Give the extent of all Plasmodium vivax-infected red blood cells.
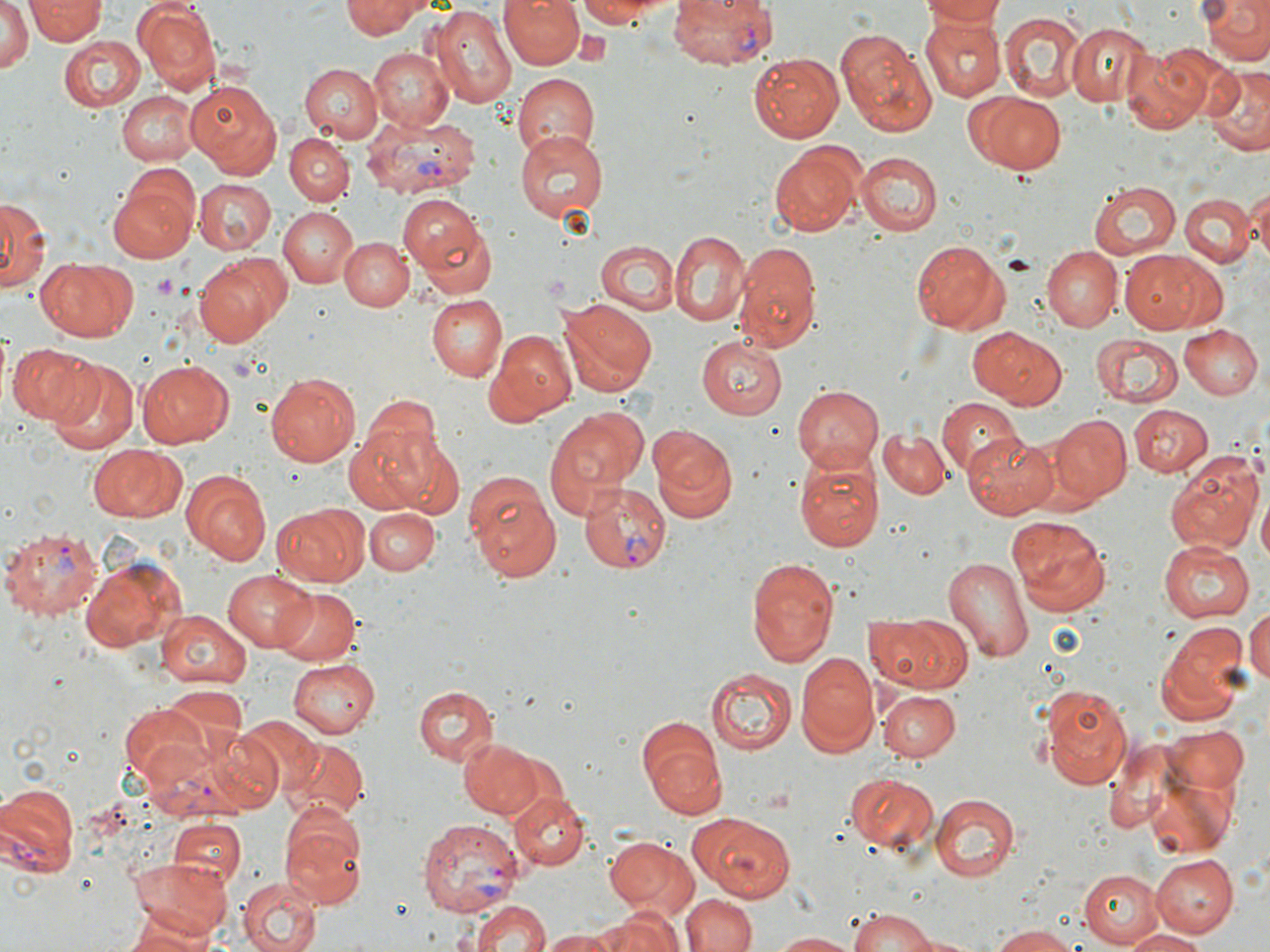
Approximate bounding boxes as (x1, y1, x2, y2) in pixels.
Plasmodium vivax-infected red blood cells: (667, 0, 778, 71), (361, 110, 480, 199), (578, 482, 672, 573), (1, 524, 104, 616), (137, 728, 276, 818), (0, 784, 79, 883), (418, 816, 523, 919).

Uninfected red blood cell locations: (26, 0, 105, 43), (339, 0, 426, 37), (501, 0, 586, 71), (573, 0, 676, 26), (918, 0, 1008, 28), (1196, 0, 1270, 67), (132, 1, 221, 95), (0, 4, 35, 73), (430, 5, 517, 106), (997, 10, 1086, 102), (919, 17, 1004, 100), (1065, 22, 1153, 109), (833, 28, 937, 138), (56, 35, 147, 111), (369, 46, 454, 131), (1122, 46, 1214, 134), (748, 53, 845, 142), (299, 63, 383, 142), (1202, 67, 1270, 155), (512, 72, 601, 161), (185, 79, 282, 177), (117, 90, 198, 166), (976, 93, 1068, 174), (514, 130, 608, 224), (286, 131, 355, 205), (769, 143, 864, 237), (854, 152, 941, 236), (107, 178, 199, 264), (191, 178, 276, 254), (1088, 179, 1181, 260), (1244, 188, 1269, 265), (1182, 193, 1254, 267), (0, 195, 47, 294), (397, 195, 487, 276), (279, 207, 359, 287), (415, 214, 499, 300), (668, 229, 747, 326), (339, 237, 414, 311), (911, 240, 1011, 334), (595, 241, 678, 313), (734, 242, 822, 352), (1043, 248, 1121, 331), (1119, 251, 1213, 332), (195, 253, 291, 346), (35, 257, 138, 343), (426, 295, 507, 383), (560, 298, 655, 395), (1178, 325, 1262, 399), (968, 327, 1069, 411), (491, 330, 577, 419), (1090, 334, 1184, 408), (696, 336, 788, 420), (5, 343, 93, 427), (134, 359, 233, 448), (45, 360, 140, 455), (264, 372, 362, 466), (791, 384, 883, 472), (361, 389, 443, 465), (935, 399, 1022, 476), (1128, 403, 1211, 479), (543, 406, 646, 519), (1048, 414, 1132, 503), (648, 424, 738, 521), (344, 426, 442, 514), (877, 427, 952, 500), (963, 429, 1057, 516), (89, 445, 182, 522), (792, 450, 884, 552), (1166, 456, 1263, 550), (462, 468, 562, 582), (185, 471, 273, 566), (1258, 493, 1270, 575), (273, 502, 368, 587), (366, 508, 441, 577), (1008, 514, 1112, 614), (1158, 542, 1254, 622), (944, 552, 1036, 665), (747, 555, 840, 668), (83, 557, 180, 653), (222, 568, 319, 653), (272, 586, 362, 664), (1244, 604, 1270, 691), (155, 611, 251, 688), (868, 614, 975, 695), (1154, 620, 1254, 726), (795, 650, 879, 755), (286, 657, 381, 737), (705, 669, 798, 753), (1041, 683, 1133, 791), (413, 685, 498, 768), (877, 687, 960, 762), (120, 702, 216, 791), (234, 715, 322, 799), (1164, 725, 1251, 792), (458, 737, 541, 819), (640, 737, 731, 823), (1102, 737, 1183, 837), (281, 741, 367, 826), (1146, 771, 1240, 858), (845, 772, 938, 855), (510, 792, 589, 871), (931, 792, 1020, 881), (279, 809, 368, 909), (690, 810, 797, 903), (168, 818, 243, 890), (605, 835, 700, 921), (1152, 855, 1237, 937), (128, 856, 231, 942), (1078, 868, 1165, 948), (236, 876, 322, 952), (683, 893, 756, 952), (466, 894, 552, 951), (595, 906, 682, 952), (846, 909, 942, 952), (123, 920, 219, 952), (988, 925, 1087, 951), (1123, 929, 1211, 951), (543, 930, 615, 952), (769, 930, 861, 951), (896, 930, 987, 950). Platelet locations: (152, 273, 181, 299). Slide-level diagnosis: Plasmodium vivax. Image is 1270×952 pixels. Thin blood smear. One field of a larger specimen. Light microscopy. May-Grünwald-Giemsa-stained preparation. 1000x magnification.